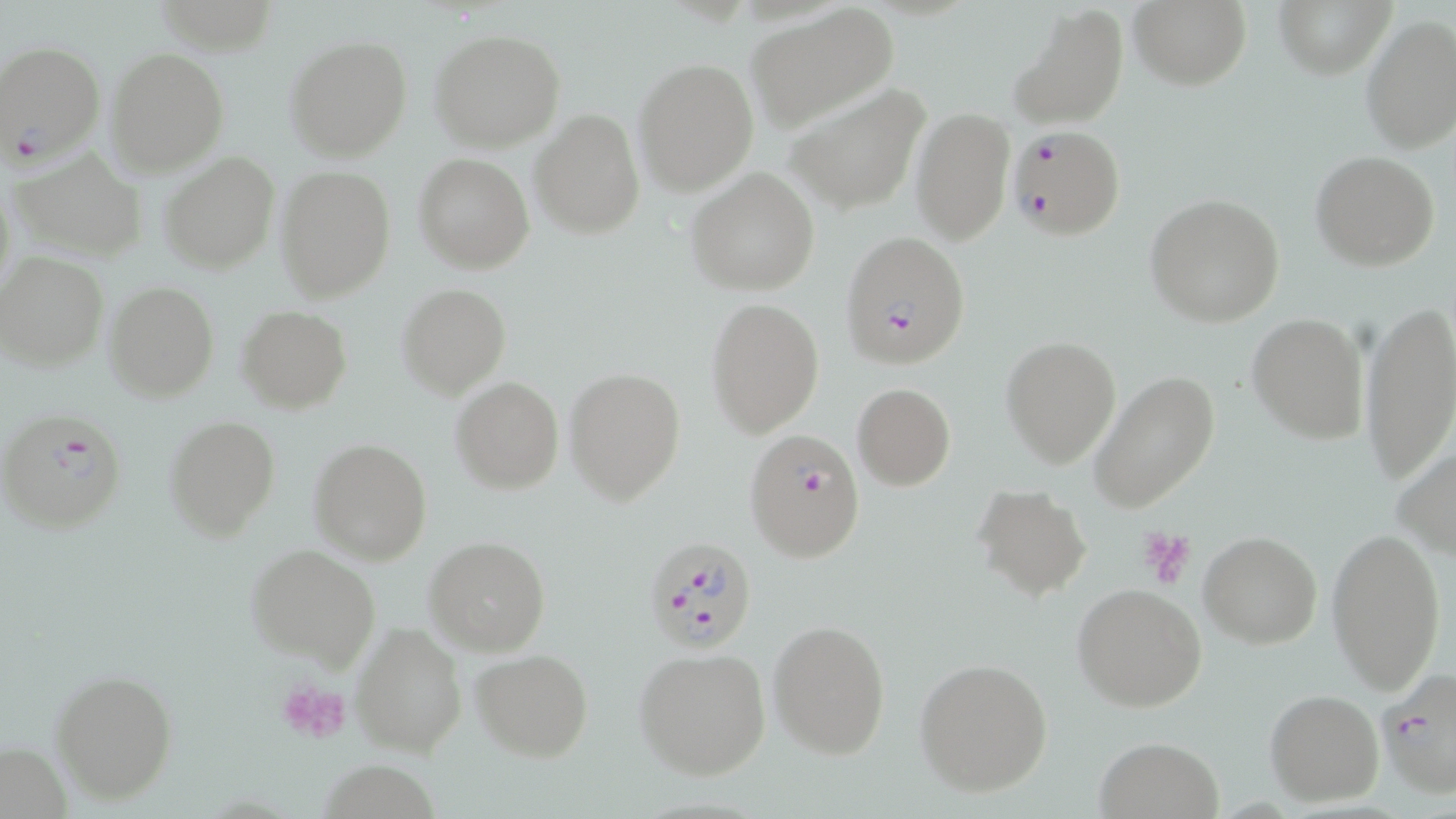
Plasmodium falciparum-infected red blood cell locations = approximate bounding boxes as (x1, y1, x2, y2) in pixels: (0, 40, 106, 170), (1007, 125, 1127, 241), (841, 232, 970, 369), (1, 408, 127, 534), (744, 428, 866, 564), (643, 536, 760, 656), (1374, 666, 1456, 799)
slide-level diagnosis = Plasmodium falciparum
magnification = 1000x
image size = 1456×819 pixels
preparation = thin blood smear
stain = May-Grünwald-Giemsa
platelet locations = approximate bounding boxes as (x1, y1, x2, y2) in pixels: (1138, 526, 1198, 593), (278, 679, 353, 745)
field of view = single
uninfected red blood cell locations = approximate bounding boxes as (x1, y1, x2, y2) in pixels: (1130, 0, 1251, 90), (1273, 0, 1391, 78), (744, 3, 899, 133), (1008, 3, 1130, 132), (1359, 17, 1456, 156), (429, 28, 567, 152), (284, 35, 412, 162), (105, 46, 229, 177), (634, 57, 758, 196), (783, 81, 931, 215), (910, 107, 1015, 244), (531, 109, 644, 238), (10, 148, 147, 263), (1311, 151, 1441, 272), (159, 152, 280, 275), (414, 153, 534, 273), (275, 166, 396, 302), (687, 167, 820, 297), (1144, 194, 1285, 326), (1, 252, 111, 371), (104, 282, 220, 402), (397, 283, 511, 398), (705, 296, 823, 438), (1359, 299, 1456, 482), (238, 306, 351, 414), (1247, 313, 1367, 443), (1001, 336, 1121, 469), (564, 366, 687, 504), (1088, 371, 1221, 514), (451, 377, 563, 494), (852, 382, 955, 491), (163, 415, 281, 541), (310, 438, 431, 565), (1394, 442, 1456, 562), (973, 484, 1091, 601), (1326, 524, 1448, 696), (1197, 531, 1323, 649), (424, 536, 551, 657), (246, 546, 380, 670), (1073, 584, 1207, 713), (768, 618, 891, 759), (352, 621, 466, 756), (633, 648, 772, 779), (471, 649, 594, 761), (915, 658, 1054, 797), (51, 668, 177, 803), (1264, 688, 1383, 806), (1090, 737, 1225, 819)
modality = optical microscopy